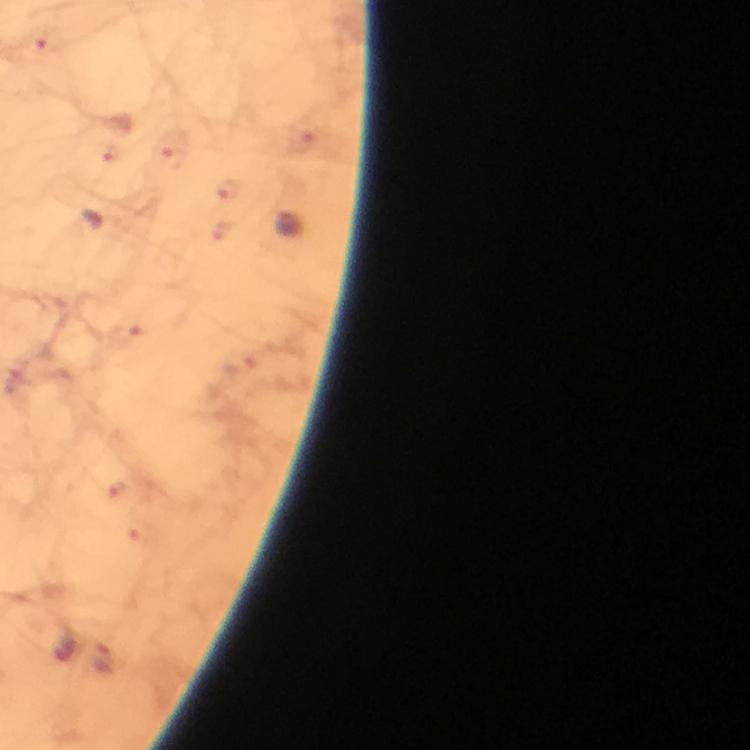
Approximate centers as (x, y) in pixels. Malaria parasite locations: (47, 42), (176, 151), (111, 153), (227, 191), (125, 332), (102, 660). From a malaria diagnostic workup. Cropped region of a single field of view. Image is 750×750 pixels. Photographed with a smartphone mounted on the microscope. Immersion oil was used. 100x magnification. Giemsa-stained preparation. Thick blood smear.